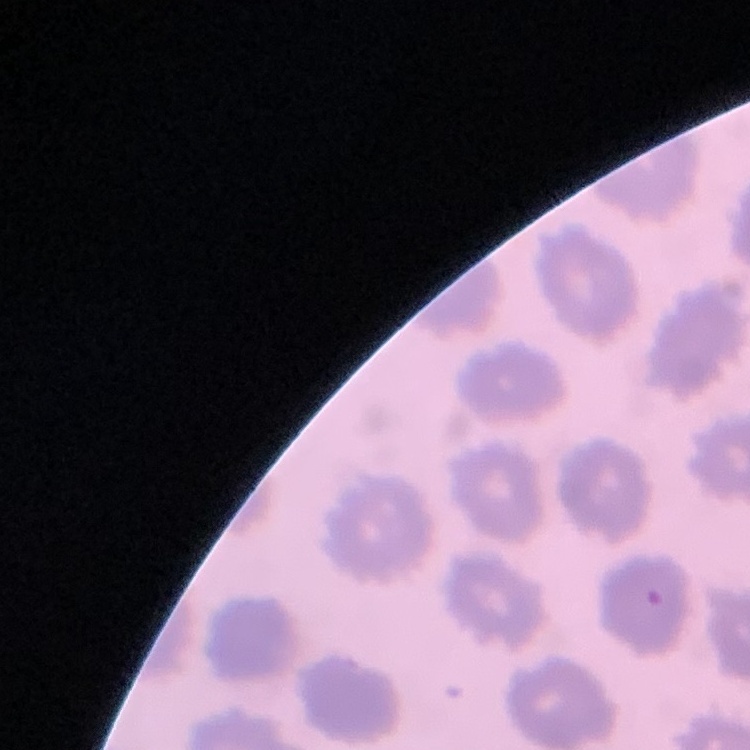
Summary:
  - Red blood cell morphology: no rouleaux formation
  - Preparation: thin peripheral smear
  - Stain: Field's or Giemsa
  - Image type: one tile cut from a larger photomicrograph